Name the cell type shown.
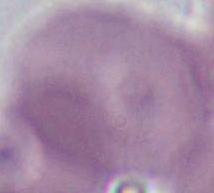

An erythrocyte.

Summary:
  - Modality: micrograph
  - Magnification: 1000x